State which parasite is depicted.
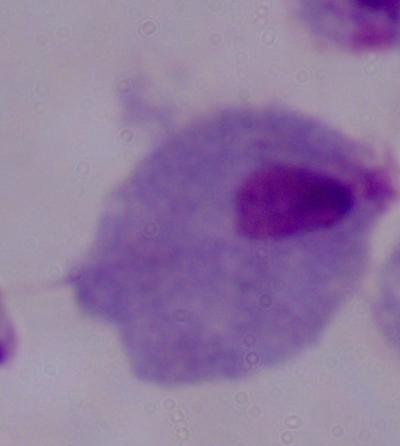
A trichomonad.

{
  "magnification": "1000x",
  "modality": "micrograph"
}